Assess the background quality.
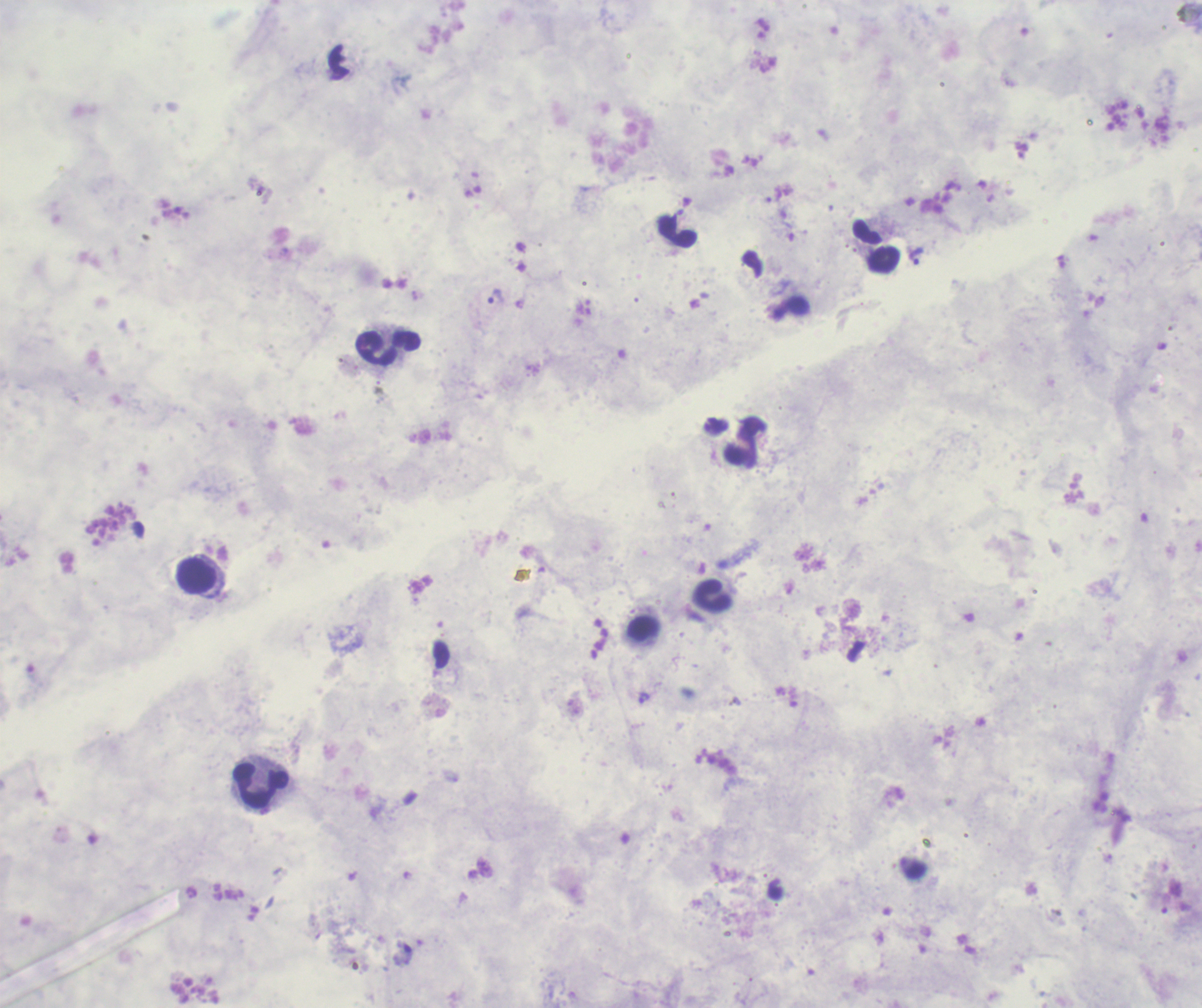

It is poor.

coordinate format = approximate object centers, in pixels from the top-left corner
leukocyte locations = (x=677, y=233), (x=388, y=347), (x=196, y=575), (x=261, y=786)
trophozoite locations = (x=916, y=256), (x=496, y=297), (x=712, y=597), (x=644, y=698)
result = Plasmodium parasites identified
preparation = thick blood smear
field of view = single
context = previously used in a real diagnosis
image size = 1202×1008 pixels
magnification = 100x
stain = Romanowsky